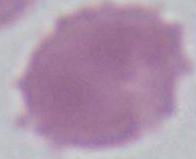
modality = micrograph
magnification = 1000x
identification = erythrocyte